Name the parasite shown.
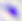
This is Toxoplasma gondii.

magnification: 400x
modality: micrograph